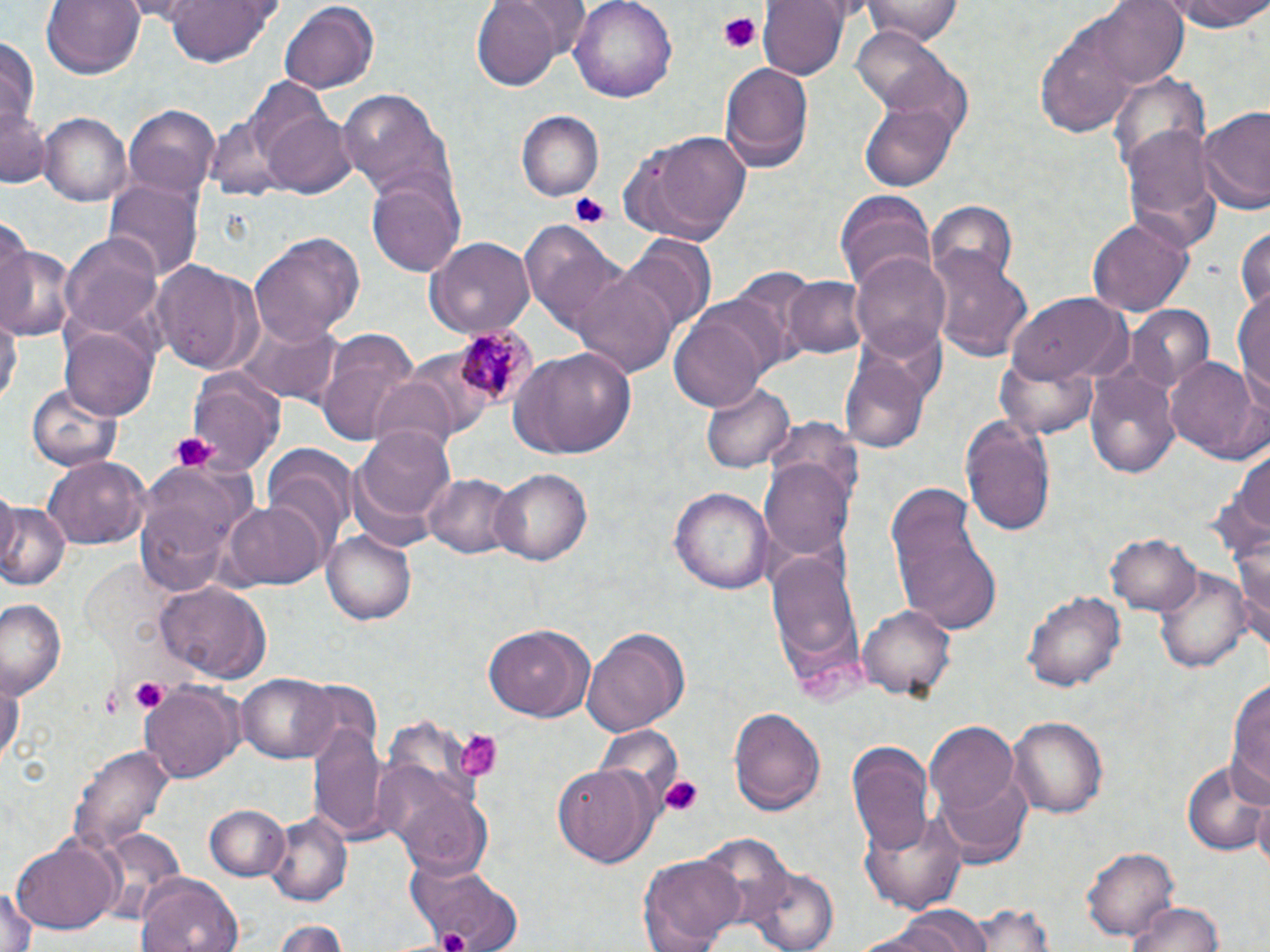

plasmodium_malariae_infected_red_blood_cell_locations: 'approximate bounding boxes as (x1,y1)-(x2,y2) corner pairs in pixels: (452,322)-(542,415)'
slide_level_diagnosis: Plasmodium malariae
stain: May-Grünwald-Giemsa
magnification: 1000x
image_size: 1270×952 pixels
uninfected_red_blood_cell_locations: 'approximate bounding boxes as (x1,y1)-(x2,y2) corner pairs in pixels: (40,0)-(146,79), (160,0)-(280,68), (470,0)-(562,90), (568,0)-(678,104), (758,0)-(848,79), (863,0)-(963,44), (1090,0)-(1188,89), (1160,0)-(1270,33), (278,2)-(380,94), (1035,15)-(1138,138), (851,27)-(966,121), (1,39)-(40,124), (718,62)-(814,175), (1108,71)-(1208,177), (338,88)-(452,201), (860,100)-(957,190), (1,103)-(50,188), (1196,104)-(1270,217), (123,106)-(220,198), (262,108)-(357,199), (516,111)-(603,201), (40,113)-(130,204), (205,114)-(291,200), (1120,118)-(1219,240), (620,130)-(752,247), (369,179)-(463,275), (105,182)-(202,286), (834,190)-(935,294), (927,203)-(1018,290), (1086,216)-(1193,319), (1233,224)-(1270,313), (524,227)-(633,337), (63,232)-(165,337), (249,232)-(365,343), (619,235)-(714,331), (427,236)-(534,339), (0,242)-(74,341), (930,249)-(1031,362), (850,250)-(951,360), (151,263)-(264,375), (573,271)-(681,384), (783,276)-(869,357), (1233,285)-(1270,403), (1007,293)-(1133,385), (1125,305)-(1213,394), (667,307)-(776,413), (0,314)-(19,412), (231,316)-(344,405), (59,326)-(157,420), (313,329)-(421,444), (508,347)-(637,459), (1166,355)-(1266,465), (839,356)-(928,455), (998,359)-(1097,441), (1083,365)-(1182,483), (185,372)-(282,480), (371,381)-(455,474), (702,381)-(793,473), (26,384)-(120,471), (960,415)-(1057,536), (354,422)-(456,528), (1225,443)-(1268,553), (265,445)-(356,551), (41,457)-(148,549), (759,458)-(854,563), (135,460)-(254,593), (488,468)-(595,567), (423,473)-(519,559), (672,483)-(775,590), (884,484)-(1003,633), (225,498)-(327,590), (0,501)-(69,592), (1229,518)-(1270,640), (323,530)-(419,626), (1108,534)-(1202,617), (767,549)-(864,688), (1154,560)-(1249,675), (155,580)-(273,682), (1024,588)-(1125,694), (1,599)-(67,694), (860,605)-(957,699), (483,622)-(594,723), (581,624)-(691,735), (0,668)-(23,770), (237,671)-(340,764), (1227,674)-(1270,804), (141,681)-(243,782), (728,707)-(826,816), (1007,714)-(1107,818), (308,717)-(388,842), (927,721)-(1021,819), (847,740)-(939,854), (71,744)-(173,858), (1181,757)-(1267,854), (553,763)-(661,865), (934,771)-(1033,861), (392,785)-(492,875), (1251,796)-(1270,877), (204,804)-(289,882), (860,807)-(968,913), (267,810)-(353,904), (91,825)-(186,922), (8,836)-(122,937), (1084,846)-(1180,938), (639,852)-(743,952), (411,864)-(522,952), (748,867)-(842,952), (137,872)-(243,952), (0,882)-(38,952), (962,901)-(1061,952), (1123,901)-(1228,952), (863,909)-(997,951), (275,917)-(349,951)'
field_of_view: one of a larger specimen
platelet_locations: 'approximate bounding boxes as (x1,y1)-(x2,y2) corner pairs in pixels: (716,10)-(763,52), (569,191)-(611,229), (167,430)-(217,472), (130,678)-(168,716), (100,686)-(128,716), (454,729)-(502,779), (654,776)-(704,818)'
preparation: thin blood film
modality: optical microscopy